Describe the morphology of the erythrocytes.
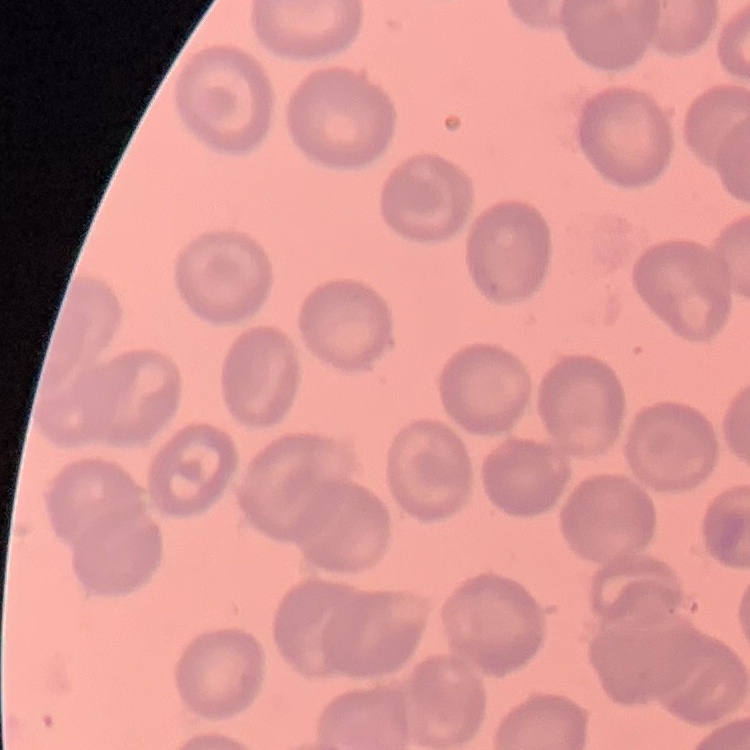

No rouleaux formation.

Summary:
  - Image type: square crop of a larger photomicrograph
  - Stain: Field's or Giemsa
  - Preparation: thin blood film